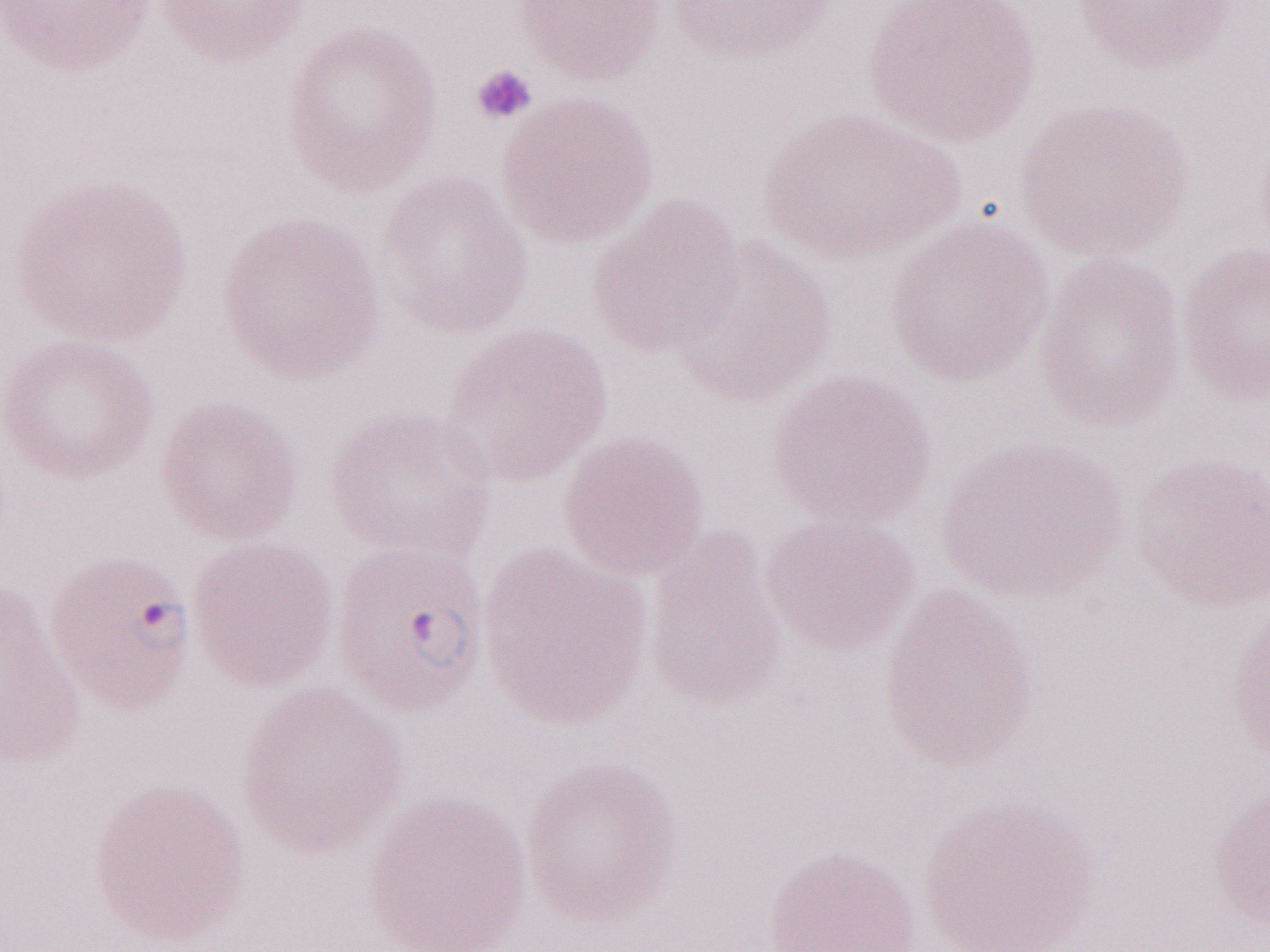

Image is 1270×952 pixels. 1,000x magnification. One field of this slide. Olympus BX43 microscope, Olympus DP73 camera. May-Grünwald-Giemsa-stained preparation. Malaria diagnosis (patient-level): positive. Thin blood film.